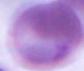
Micrograph. A red blood cell is shown. 1000x magnification.